Outline each blood parasite and name the species.
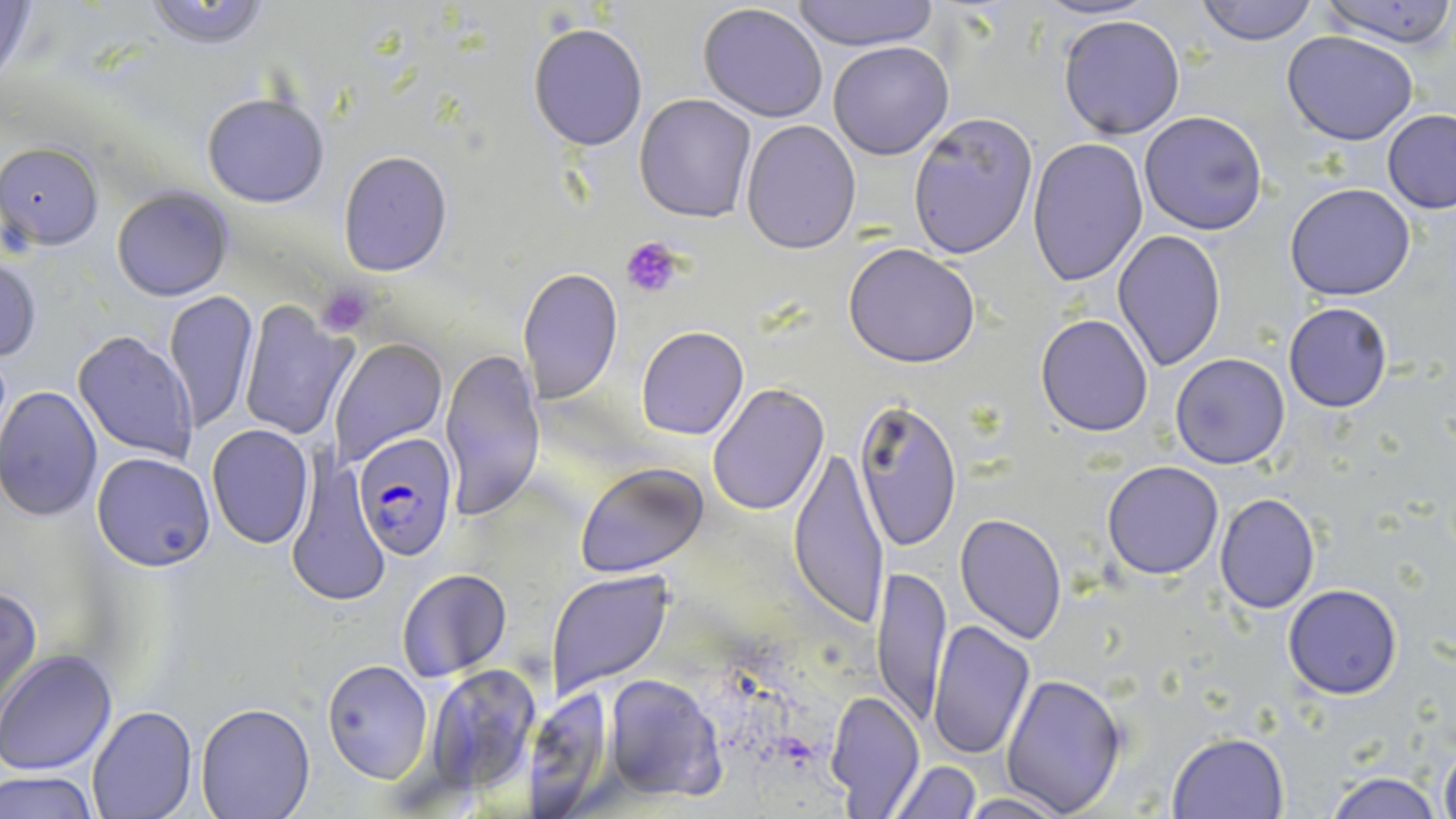
Approximate bounding boxes as [x1, y1, x2, y2] in pixels.
Plasmodium falciparum-infected red blood cells: [355, 435, 456, 558].
No Plasmodium ovale, Plasmodium malariae, Plasmodium vivax, Babesia divergens, or Trypanosoma brucei observed.

Uninfected red blood cell locations: [787, 0, 941, 50], [1037, 0, 1152, 23], [1194, 0, 1319, 45], [1317, 0, 1455, 48], [141, 1, 278, 50], [0, 2, 43, 89], [697, 2, 829, 123], [1058, 13, 1185, 140], [528, 22, 648, 151], [1282, 30, 1419, 145], [828, 40, 955, 160], [202, 93, 330, 208], [635, 94, 758, 223], [1139, 110, 1268, 235], [1382, 110, 1456, 213], [907, 113, 1038, 261], [740, 118, 862, 254], [1026, 138, 1148, 287], [1, 141, 104, 249], [337, 151, 453, 276], [1284, 182, 1416, 301], [112, 187, 232, 301], [1113, 229, 1227, 371], [843, 242, 982, 368], [0, 254, 42, 362], [516, 268, 623, 404], [163, 290, 261, 433], [236, 301, 355, 442], [1283, 301, 1393, 413], [1035, 313, 1154, 436], [637, 325, 748, 441], [75, 330, 200, 462], [330, 337, 447, 466], [439, 348, 546, 520], [1171, 353, 1290, 470], [708, 383, 831, 517], [0, 384, 102, 522], [852, 395, 962, 551], [205, 424, 314, 548], [787, 444, 892, 630], [90, 451, 216, 572], [1101, 461, 1224, 581], [575, 462, 709, 580], [288, 468, 391, 609], [1214, 491, 1320, 612], [954, 514, 1069, 643], [872, 561, 951, 731], [397, 568, 511, 682], [547, 569, 675, 700], [0, 584, 42, 713], [1282, 584, 1403, 700], [926, 619, 1035, 762], [0, 649, 119, 775], [321, 660, 434, 783], [424, 664, 544, 793], [602, 673, 727, 803], [1001, 673, 1128, 815], [524, 686, 615, 814], [824, 690, 927, 816], [195, 702, 316, 819], [86, 706, 197, 818], [1168, 733, 1290, 819], [1438, 741, 1456, 819], [887, 760, 982, 818], [3, 771, 99, 819], [1324, 772, 1442, 819], [953, 792, 1075, 818]. Platelet locations: [621, 235, 689, 299], [316, 284, 376, 337]. Slide-level diagnosis: Plasmodium falciparum. Single field of view. Thin blood film. Captured at 1000x magnification. May-Grünwald-Giemsa stain. Image is 1456×819 pixels. Optical microscopy.